Outline each blood parasite and name the species.
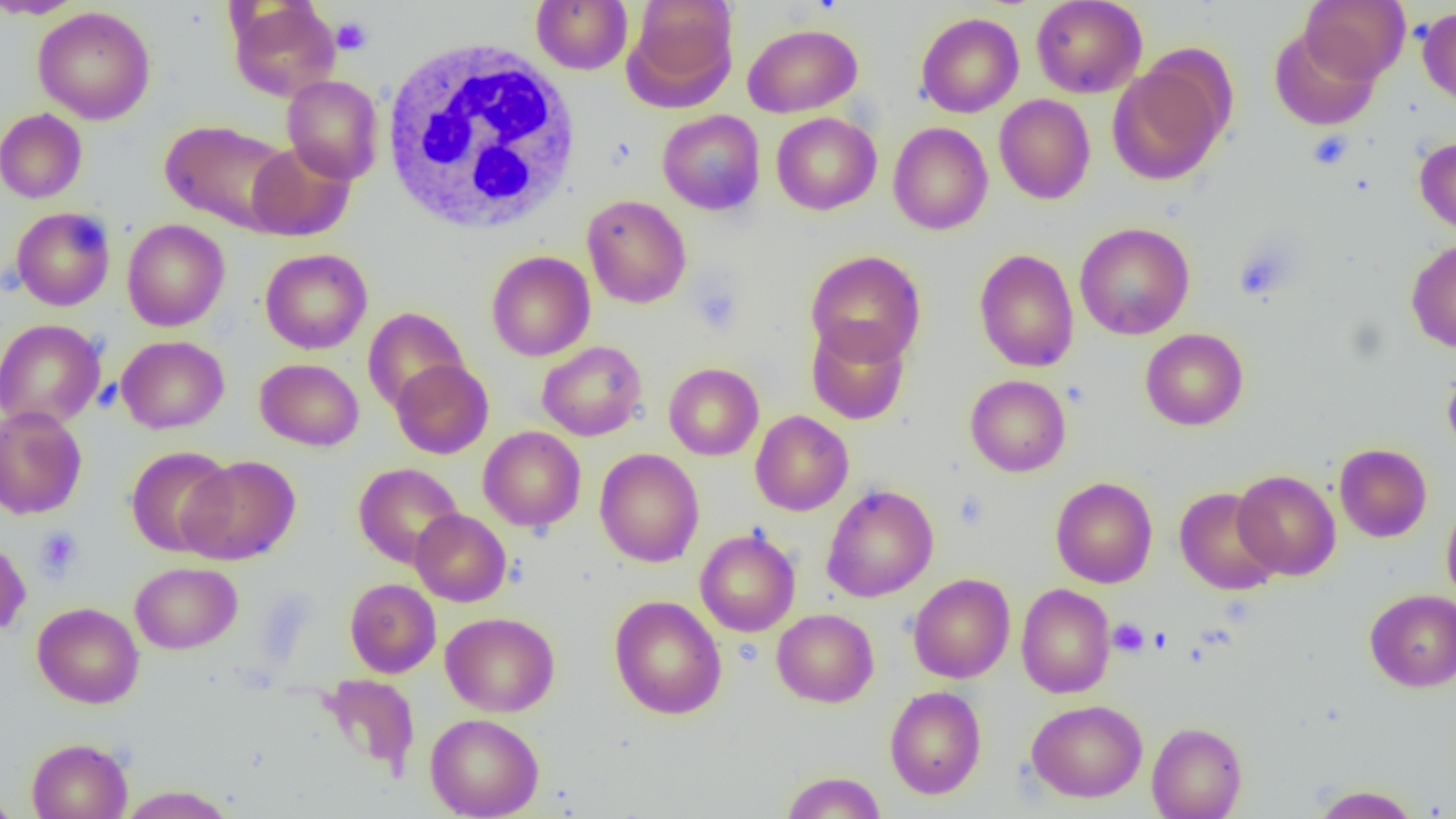
No blood parasites observed.

Approximate bounding boxes as (x1, y1, x2, y2) in pixels. Uninfected red blood cell locations: (0, 0, 86, 19), (531, 0, 632, 74), (624, 0, 738, 106), (1031, 0, 1147, 98), (1300, 0, 1410, 83), (228, 1, 340, 102), (33, 6, 155, 124), (1417, 6, 1456, 109), (916, 12, 1024, 118), (743, 23, 862, 117), (1269, 27, 1380, 131), (1107, 59, 1229, 185), (282, 75, 384, 184), (994, 94, 1095, 204), (0, 108, 87, 203), (657, 109, 765, 215), (771, 112, 882, 215), (160, 120, 295, 234), (889, 122, 993, 235), (1414, 136, 1456, 237), (246, 142, 356, 241), (582, 195, 691, 309), (10, 206, 116, 311), (122, 218, 230, 332), (1075, 222, 1194, 340), (1406, 238, 1456, 353), (260, 248, 372, 354), (974, 249, 1079, 372), (806, 250, 926, 366), (486, 251, 595, 361), (363, 307, 469, 413), (0, 319, 106, 429), (806, 320, 910, 425), (1140, 328, 1248, 430), (116, 335, 229, 434), (537, 341, 647, 441), (255, 358, 364, 451), (390, 359, 494, 459), (664, 362, 764, 461), (1442, 365, 1456, 460), (965, 375, 1071, 477), (0, 406, 87, 520), (750, 411, 853, 515), (478, 426, 586, 531), (1334, 443, 1432, 542), (125, 446, 235, 557), (594, 448, 704, 568), (178, 455, 300, 565), (353, 462, 464, 568), (1232, 470, 1341, 580), (1051, 476, 1158, 588), (821, 485, 938, 602), (1174, 487, 1282, 595), (1441, 498, 1456, 606), (411, 509, 511, 607), (695, 528, 801, 637), (0, 538, 31, 636), (130, 562, 242, 654), (909, 573, 1015, 683), (345, 578, 441, 678), (1016, 583, 1115, 699), (1365, 589, 1456, 692), (609, 595, 727, 719), (32, 602, 144, 708), (772, 609, 879, 707), (441, 612, 559, 717), (317, 674, 420, 778), (885, 686, 986, 799), (1026, 699, 1147, 802), (425, 712, 544, 819), (1147, 722, 1247, 819), (26, 737, 133, 819), (780, 771, 887, 818), (116, 784, 236, 819), (1310, 784, 1421, 818), (0, 787, 20, 819). Platelet locations: (332, 17, 372, 55), (1308, 130, 1353, 170), (1232, 237, 1300, 302), (689, 277, 743, 335), (953, 489, 990, 530), (35, 527, 83, 581), (1109, 618, 1149, 657). White blood cell locations: (379, 36, 583, 234). Slide-level diagnosis: no evidence of blood parasites. Captured at 1000x magnification. Image is 1456×819 pixels. Light microscopy. One field of a larger specimen. Thin blood film.